Classify this cell by malaria status.
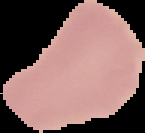

It is uninfected.

From a thin blood smear. The area outside the segmented cell region is set to black. Image is 145×133 pixels.